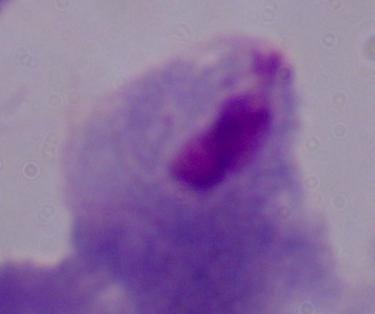
Micrograph. A trichomonad is shown. 1000x magnification.